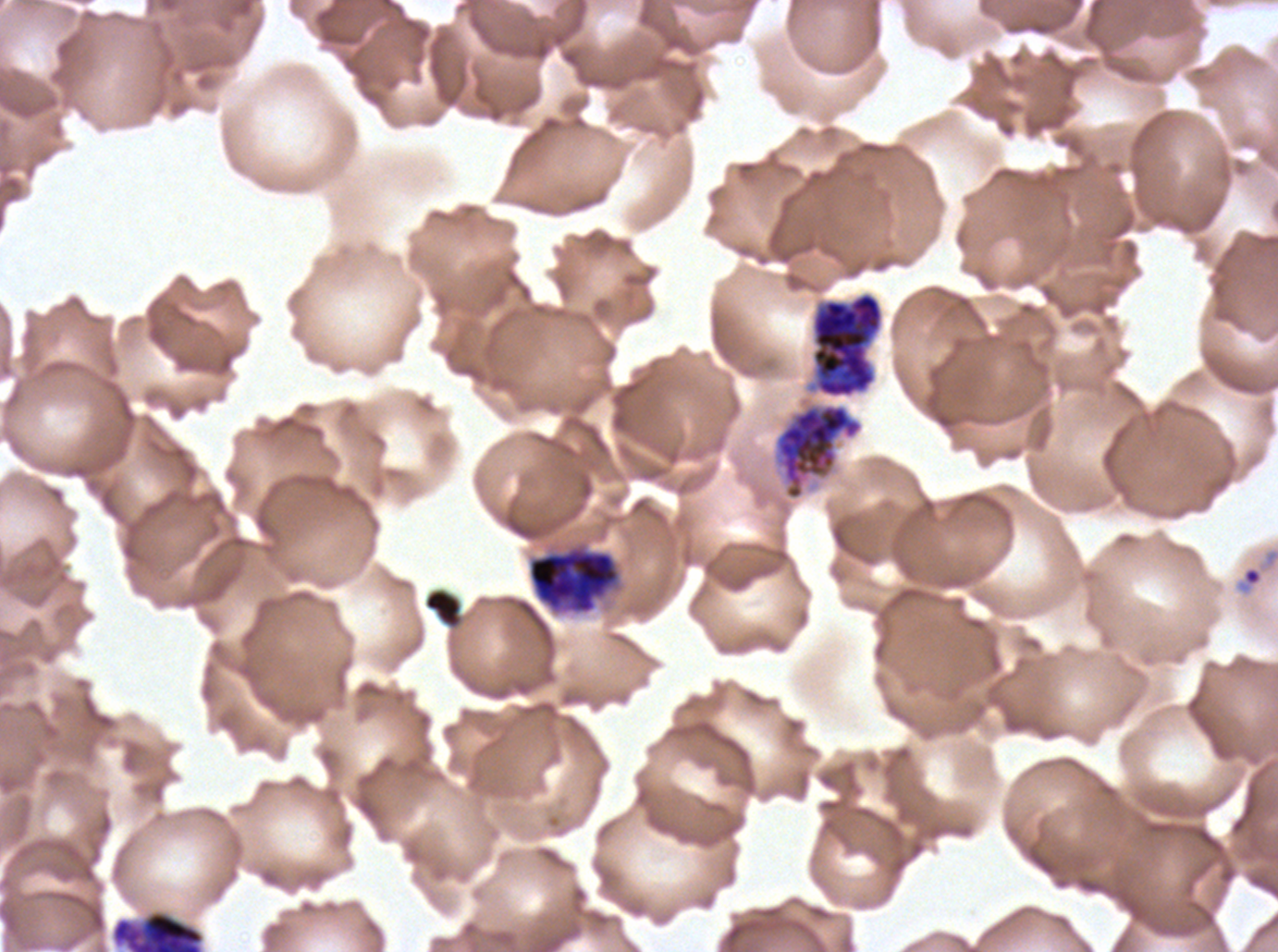
Approximate bounding boxes as {x1, y1, x2, y2} in pixels. Debris locations: {423, 587, 464, 630}. Late schizont locations: {811, 291, 884, 398}, {774, 403, 864, 500}. Early schizont locations: {527, 543, 621, 616}, {110, 909, 205, 951}. Ring locations: {1234, 546, 1277, 597}. A sub-image separated from a larger composite. Life-cycle stages observed: ring, early schizont, late schizont. Ex-vivo Plasmodium falciparum culture from a patient in The Gambia, grown for 24 to 48 hours. Image is 1278×952 pixels. Giemsa-stained preparation. Thin blood film.